Describe the morphology of the erythrocytes.
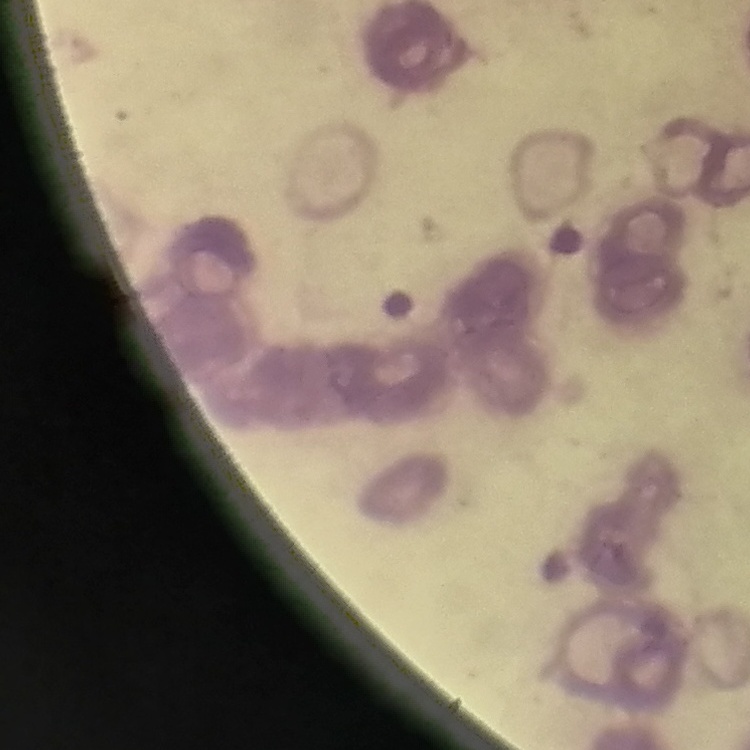

They show rouleaux formation.

stain = Field's or Giemsa
preparation = thin peripheral smear
image type = one tile cut from a larger photomicrograph